Comment on the morphology of the red blood cells.
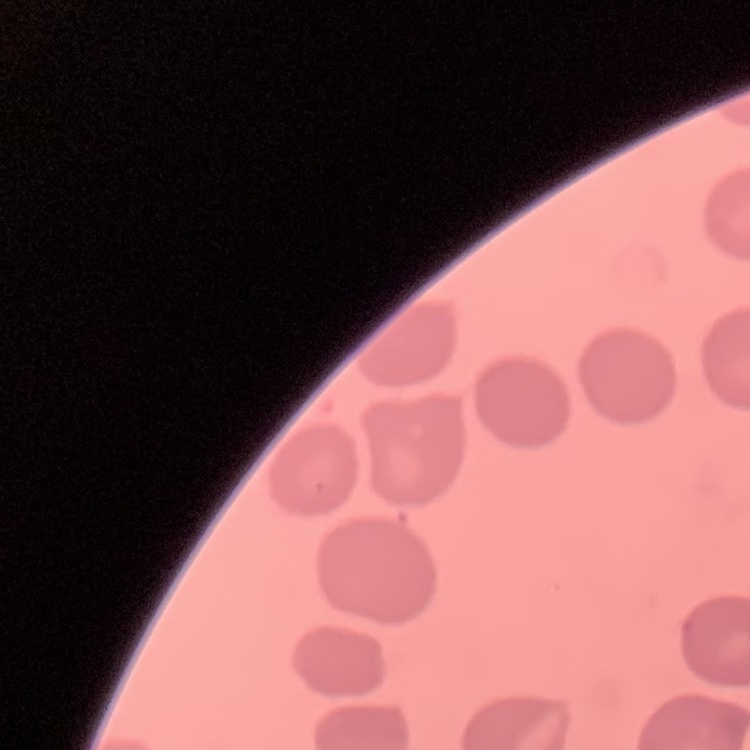

They show no rouleaux formation.

One tile cut from a larger photomicrograph. Thin blood film. Field's or Giemsa stain.